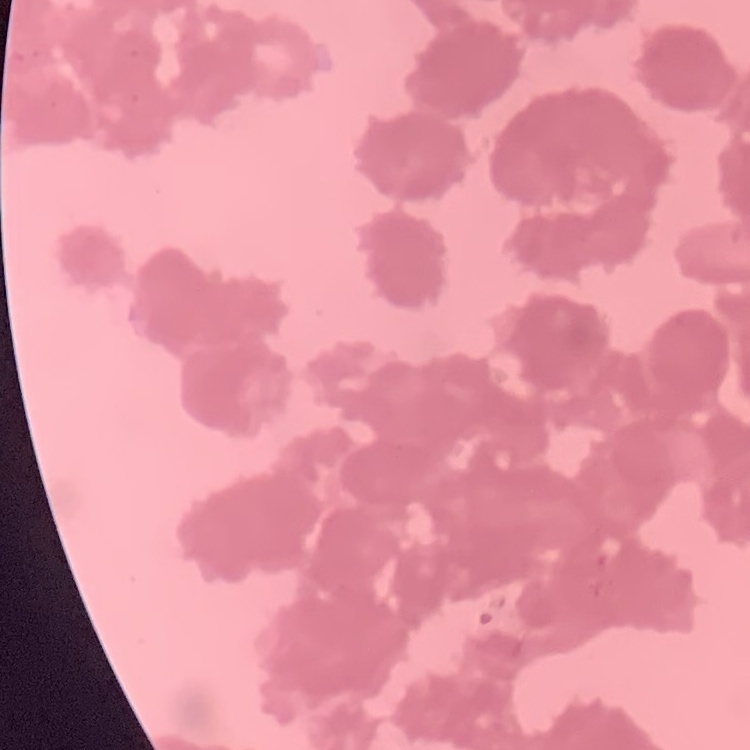

erythrocyte morphology = rouleaux formation
preparation = thin peripheral smear
image type = square crop of a larger photomicrograph
stain = Field's or Giemsa